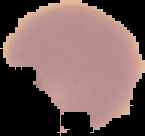

result = negative for Plasmodium parasites
preparation = thin blood film
image type = segmented cell region with the area outside set to black
image size = 145×136 pixels